Locate every blood parasite and identify its species.
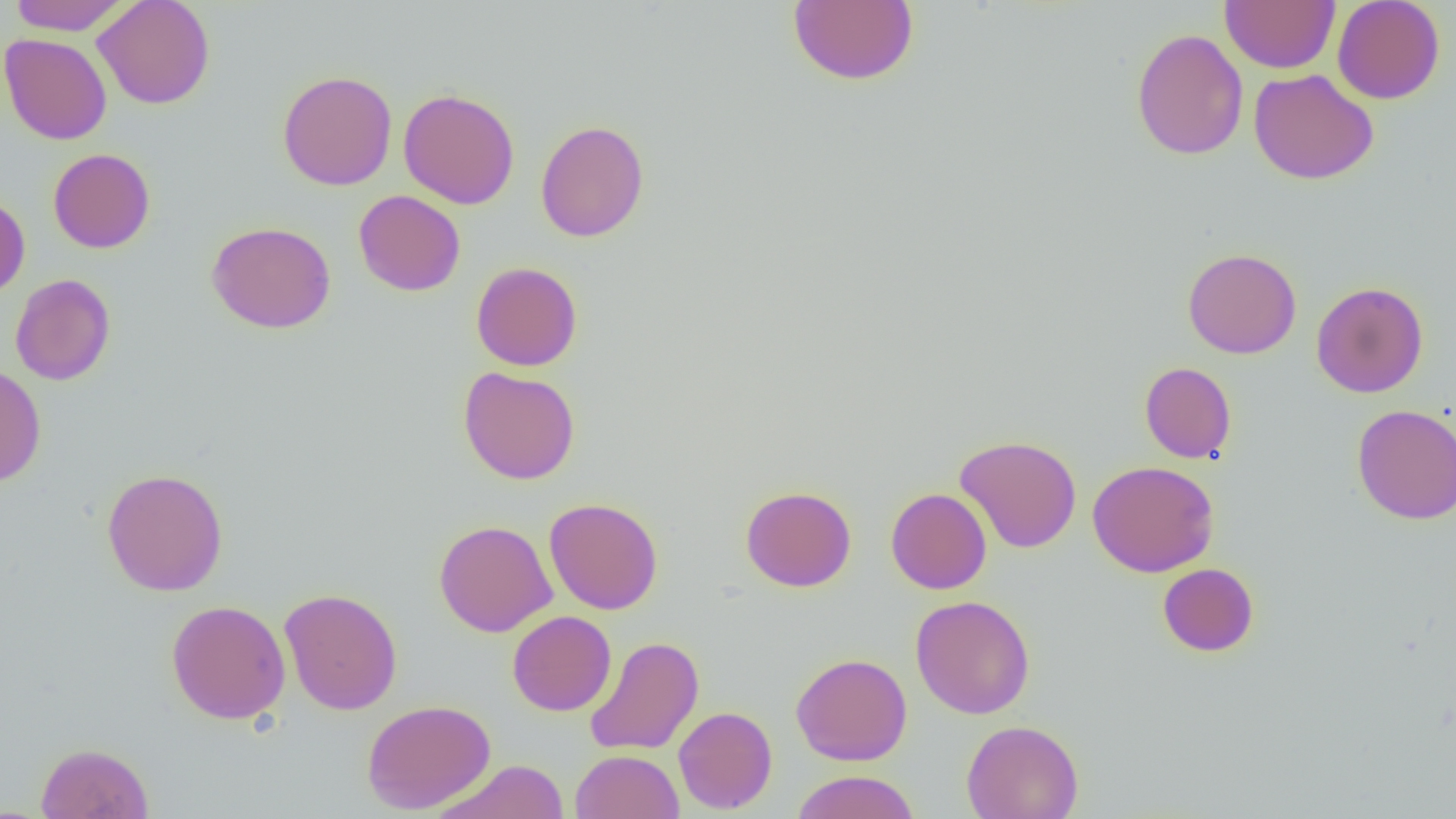
No blood parasites observed.

Approximate bounding boxes as named x1/y1/x2/y2 corners in pixels. Uninfected red blood cell locations: (x1=9, y1=0, x2=131, y2=35), (x1=92, y1=0, x2=216, y2=109), (x1=787, y1=0, x2=919, y2=86), (x1=1220, y1=0, x2=1340, y2=73), (x1=1332, y1=0, x2=1445, y2=104), (x1=1132, y1=28, x2=1248, y2=161), (x1=0, y1=32, x2=112, y2=145), (x1=1248, y1=68, x2=1379, y2=185), (x1=277, y1=69, x2=397, y2=190), (x1=276, y1=80, x2=520, y2=196), (x1=398, y1=88, x2=519, y2=209), (x1=535, y1=119, x2=650, y2=243), (x1=48, y1=148, x2=155, y2=253), (x1=353, y1=189, x2=465, y2=296), (x1=0, y1=193, x2=30, y2=298), (x1=206, y1=221, x2=336, y2=334), (x1=1182, y1=247, x2=1302, y2=359), (x1=470, y1=261, x2=582, y2=371), (x1=10, y1=273, x2=116, y2=385), (x1=1311, y1=281, x2=1428, y2=398), (x1=1139, y1=361, x2=1237, y2=464), (x1=0, y1=365, x2=46, y2=487), (x1=458, y1=366, x2=580, y2=484), (x1=1352, y1=404, x2=1456, y2=524), (x1=955, y1=435, x2=1082, y2=553), (x1=1088, y1=460, x2=1219, y2=577), (x1=101, y1=467, x2=229, y2=596), (x1=740, y1=485, x2=857, y2=592), (x1=885, y1=487, x2=992, y2=595), (x1=544, y1=497, x2=663, y2=614), (x1=433, y1=519, x2=557, y2=637), (x1=1157, y1=562, x2=1259, y2=657), (x1=279, y1=588, x2=402, y2=715), (x1=910, y1=594, x2=1035, y2=719), (x1=166, y1=600, x2=291, y2=724), (x1=507, y1=611, x2=616, y2=716), (x1=585, y1=636, x2=704, y2=756), (x1=791, y1=652, x2=913, y2=766), (x1=361, y1=699, x2=496, y2=814), (x1=673, y1=706, x2=777, y2=814), (x1=961, y1=719, x2=1084, y2=819), (x1=35, y1=742, x2=154, y2=819), (x1=570, y1=749, x2=684, y2=819), (x1=433, y1=759, x2=570, y2=818), (x1=791, y1=770, x2=921, y2=819). Slide-level diagnosis: negative for blood parasites. 1000x magnification. Image is 1456×819 pixels. Optical microscopy. One field of a larger specimen. Thin blood film.